Assess this cell for malaria.
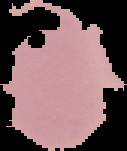
It is uninfected.

image_size: 127×151 pixels
image_type: segmented cell region with the area outside set to black
preparation: thin blood smear